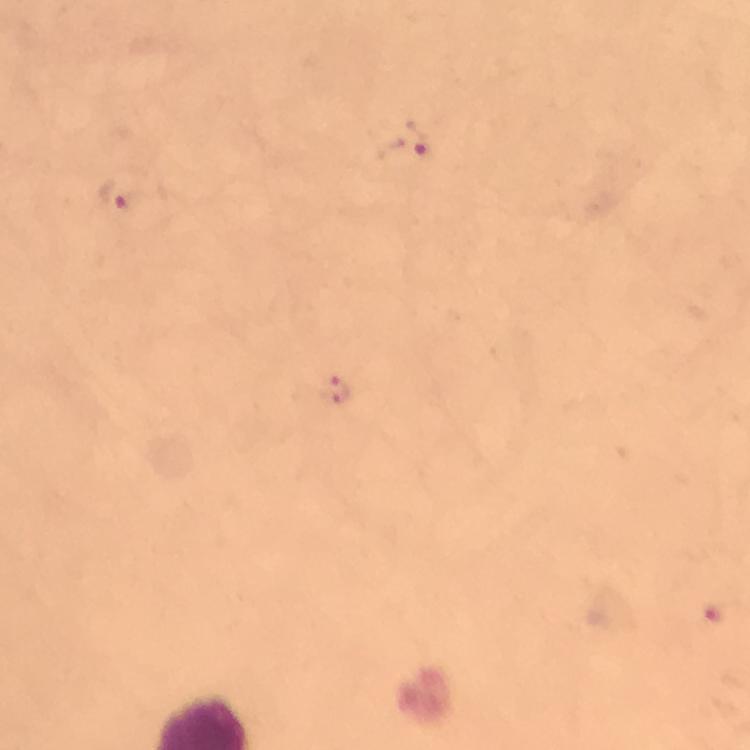
Approximate centers as [x, y] in pixels.
Summary:
  - Plasmodium parasite locations: [414, 137], [119, 197], [339, 390]
  - Capture: smartphone camera through the microscope
  - Immersion oil: used
  - Cropped from: one field of view
  - Image size: 750×750 pixels
  - Stain: Giemsa
  - Preparation: thick smear
  - Context: from a diagnostic examination for malaria
  - Magnification: 100x